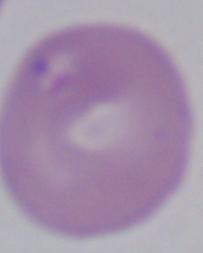

Captured at 1000x magnification. A Babesia parasite is shown. Photomicrograph.